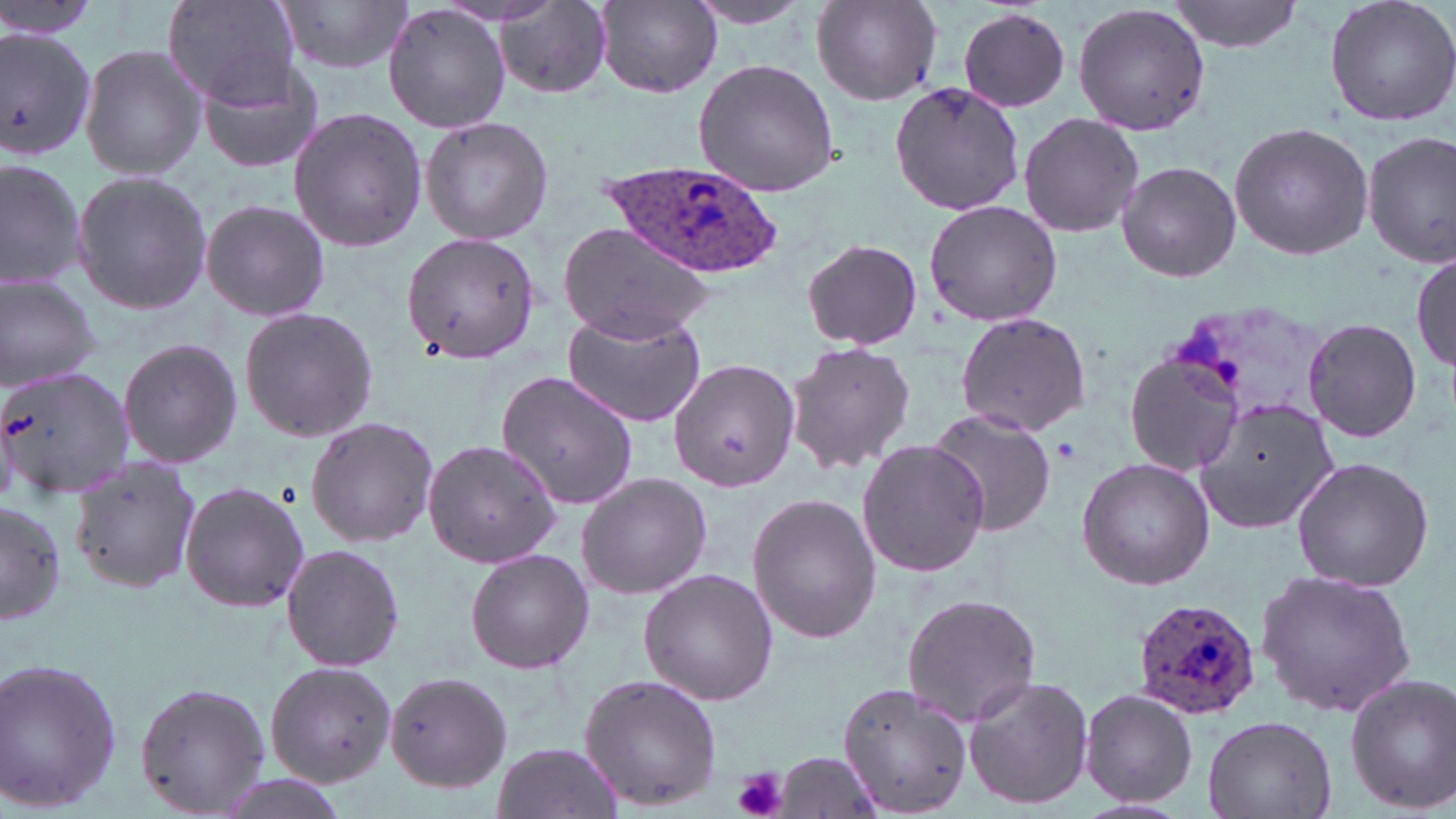
slide-level diagnosis = Plasmodium ovale
field of view = one of a larger specimen
platelet locations = approximate bounding boxes as (x1,y1)-(x2,y2) corner pairs in pixels: (1054,438)-(1082,463), (733,767)-(788,819)
Plasmodium ovale-infected red blood cell locations = approximate bounding boxes as (x1,y1)-(x2,y2) corner pairs in pixels: (602,159)-(784,277), (1131,597)-(1261,721)
preparation = thin blood smear
uninfected red blood cell locations = approximate bounding boxes as (x1,y1)-(x2,y2) corner pairs in pixels: (162,0)-(300,108), (280,0)-(414,75), (1166,0)-(1308,55), (1321,0)-(1456,129), (684,1)-(818,30), (812,1)-(942,107), (597,2)-(722,97), (493,3)-(615,98), (1074,3)-(1211,135), (382,4)-(512,135), (957,8)-(1071,112), (0,24)-(98,162), (79,43)-(206,182), (195,54)-(331,175), (691,59)-(841,197), (890,82)-(1024,215), (287,107)-(428,252), (1017,112)-(1146,238), (420,116)-(555,246), (1228,121)-(1372,261), (1362,132)-(1456,269), (0,156)-(85,291), (1115,161)-(1242,282), (70,169)-(213,315), (923,198)-(1063,327), (203,199)-(332,323), (555,222)-(716,342), (400,232)-(539,364), (801,239)-(923,349), (1413,250)-(1454,377), (0,274)-(102,391), (238,306)-(378,443), (561,311)-(706,427), (954,312)-(1091,434), (1302,316)-(1422,443), (115,336)-(245,471), (782,342)-(916,474), (1123,353)-(1247,477), (670,357)-(802,493), (0,364)-(137,500), (495,370)-(640,509), (1193,397)-(1341,535), (925,409)-(1058,535), (304,417)-(440,547), (422,438)-(564,571), (854,440)-(991,578), (69,454)-(201,594), (1290,456)-(1434,591), (1076,459)-(1214,590), (576,471)-(711,600), (180,479)-(310,613), (746,492)-(880,643), (1,498)-(65,628), (281,542)-(406,673), (465,548)-(594,675), (1256,566)-(1416,718), (637,569)-(779,704), (903,593)-(1040,726), (0,656)-(125,814), (263,660)-(399,789), (384,672)-(513,791), (578,673)-(721,812), (1344,675)-(1456,812), (964,676)-(1095,810), (134,680)-(272,819), (834,681)-(974,816), (1080,689)-(1198,808), (1202,715)-(1337,818), (493,740)-(620,816), (773,752)-(880,816), (209,773)-(355,819)
stain = May-Grünwald-Giemsa
modality = light microscopy
image size = 1456×819 pixels
magnification = 1000x